Classify this cell by malaria status.
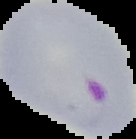

Parasitized.

From a thin blood film. Segmented cell region on a black background. Image is 136×139 pixels.